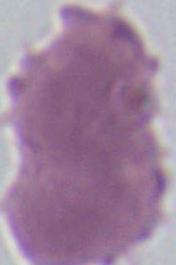

{
  "identification": "erythrocyte",
  "modality": "micrograph",
  "magnification": "1000x"
}